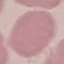

Summary:
  - Malaria status: uninfected
  - Capture: smartphone camera at the microscope eyepiece
  - Stain: Giemsa
  - Image type: automatically extracted cell patch, resized to 64 × 64 pixels
  - Preparation: thin blood film